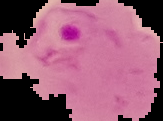 From a thin blood smear. Result: Plasmodium parasites identified. Image is 163×121 pixels. The area outside the segmented cell region is set to black.